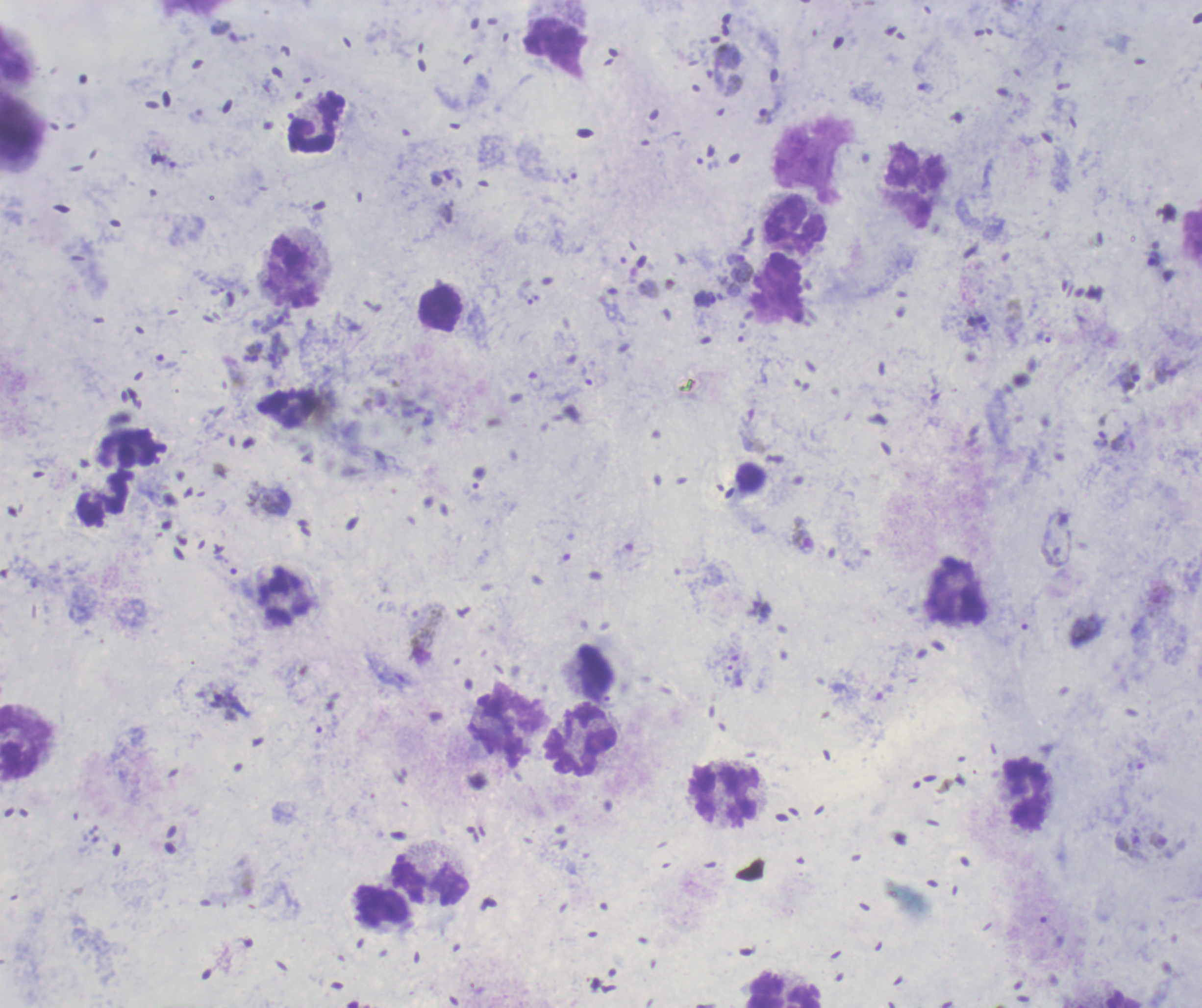

Approximate centers as [x, y] in pixels. Gametocyte locations: [802, 536], [428, 635], [1159, 840]. Trophozoite locations: [739, 268], [1045, 336], [1129, 377], [229, 705]. Leukocyte locations: [557, 48], [316, 122], [915, 188], [795, 226], [440, 310], [126, 448], [750, 478], [104, 498], [958, 593], [595, 672], [26, 741], [582, 741], [1025, 794], [724, 795], [430, 881], [383, 904], [783, 988]. Life-cycle stages observed: trophozoite, gametocyte. 100x magnification. Result: malaria parasites identified. Single field of view. Romanowsky-stained preparation. Thick blood smear. Image is 1202×1008 pixels. Background quality: satisfactory. Previously used in a real diagnosis.